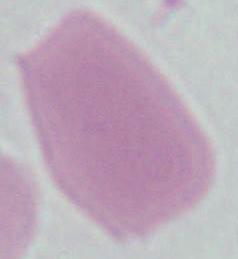

Summary:
  - Identification: red blood cell
  - Modality: photomicrograph
  - Magnification: 1000x